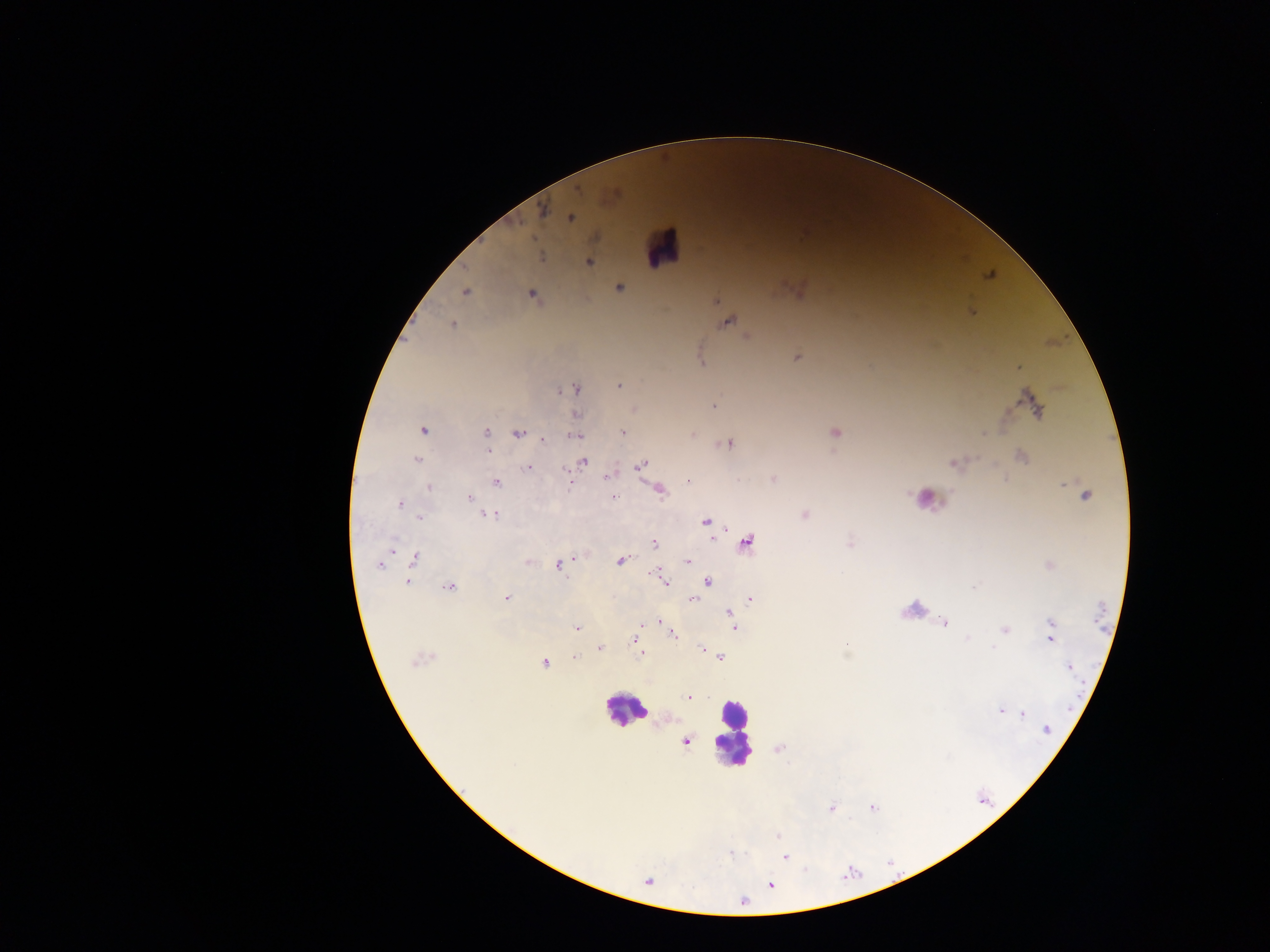
Approximate centers as x y in pixels.
Summary:
  - Leukocyte locations: 663 248; 929 503; 624 711; 732 732
  - Malaria parasite locations: 543 211; 570 217; 541 257; 589 262; 620 288; 464 293; 532 295; 716 301; 728 323; 452 324; 797 357; 702 363; 1018 367; 619 386; 575 389; 1034 405; 714 406; 576 415; 424 430; 486 432; 623 432; 836 432; 518 434; 575 435; 692 435; 543 439; 728 444; 488 450; 1022 456; 416 459; 583 462; 954 464; 640 465; 528 467; 567 471; 608 476; 773 479; 689 481; 496 483; 430 487; 660 491; 1084 494; 612 497; 468 499; 472 503; 399 505; 492 515; 804 515; 420 517; 706 522; 747 542; 654 544; 415 558; 620 561; 528 562; 688 562; 379 564; 560 566; 658 577; 663 580; 707 581; 407 582; 449 587; 973 587; 506 598; 693 600; 750 600; 730 613; 660 621; 943 622; 1052 623; 641 624; 733 624; 577 627; 1004 629; 672 634; 1051 637; 967 638; 633 639; 600 648; 994 648; 702 650; 641 653; 574 657; 720 657; 544 663; 1069 667; 689 698; 1000 710; 1022 714; 1046 729; 686 742; 872 807; 831 808; 778 836; 731 853; 784 857; 771 885; 743 902
  - Image size: 1270×952 pixels
  - Field of view: single
  - Preparation: thick blood film
  - Country: Ghana
  - Capture: mobile-phone photograph through a microscope